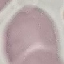
Summary:
  - Result: no malaria parasites detected
  - Stain: Giemsa
  - Image type: cell patch, automatically extracted from a larger field of view and resized to 64 × 64 pixels
  - Capture: smartphone camera at the microscope eyepiece
  - Preparation: thin smear